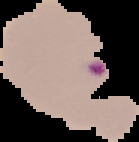

image size = 139×142 pixels
result = malaria parasites identified
preparation = thin blood smear
image type = segmented cell region on a black background